Identify the blood parasite species.
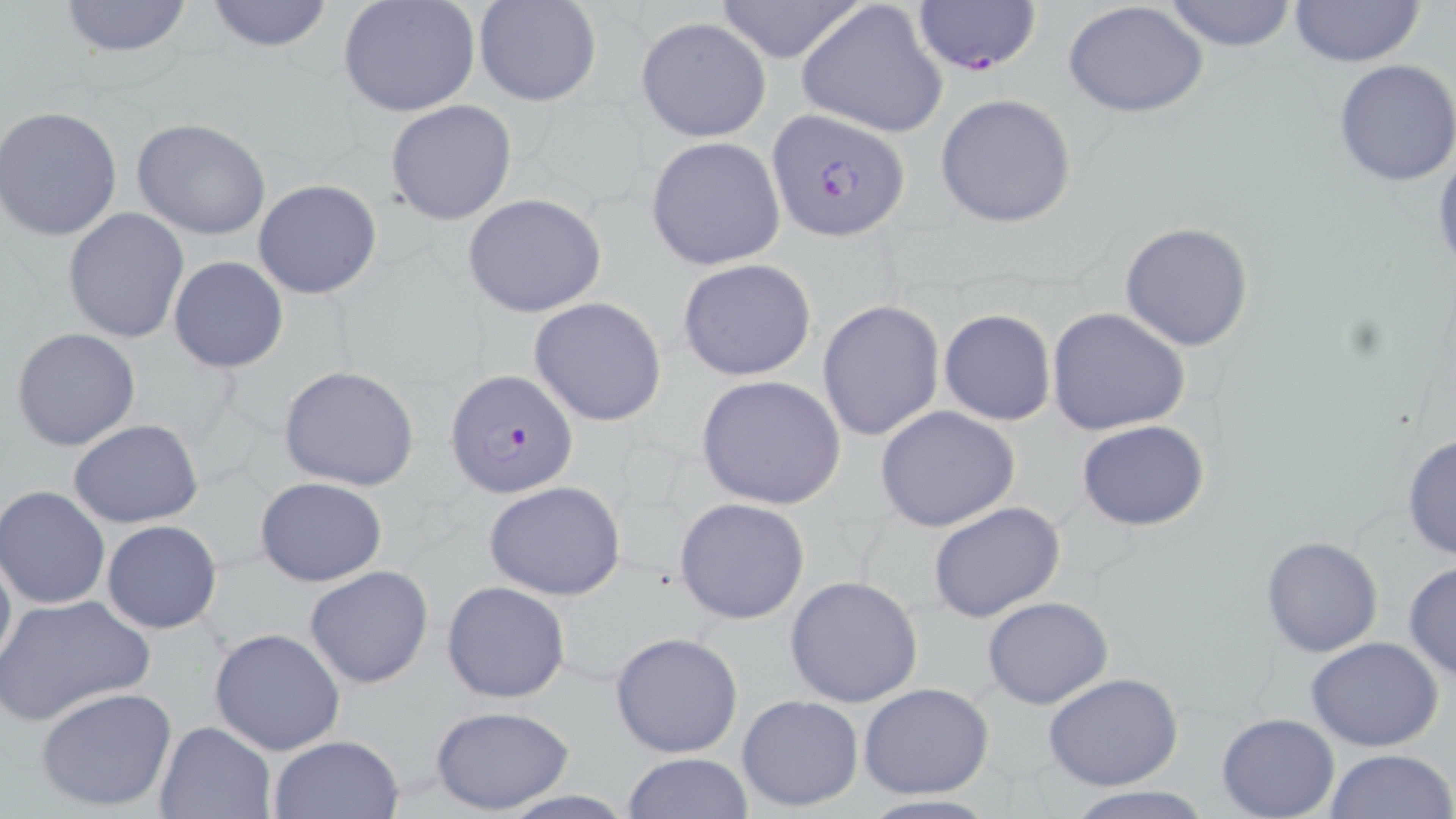
Plasmodium falciparum.

Approximate bounding boxes as (x1, y1, x2, y2) in pixels. Uninfected red blood cell locations: (56, 0, 196, 59), (204, 0, 334, 53), (338, 0, 480, 118), (474, 0, 602, 106), (708, 0, 869, 64), (796, 0, 950, 139), (1159, 0, 1300, 51), (1287, 0, 1426, 68), (1061, 1, 1212, 117), (636, 17, 770, 142), (1333, 59, 1456, 187), (935, 93, 1078, 228), (386, 99, 517, 226), (0, 105, 123, 243), (131, 119, 272, 241), (646, 137, 786, 271), (1431, 151, 1456, 280), (251, 179, 382, 300), (462, 193, 608, 318), (63, 207, 190, 343), (1119, 222, 1254, 351), (168, 257, 289, 372), (677, 258, 818, 382), (528, 297, 669, 427), (817, 298, 945, 440), (1046, 306, 1191, 436), (938, 309, 1055, 426), (10, 327, 142, 451), (278, 366, 419, 491), (695, 374, 847, 509), (875, 405, 1020, 532), (68, 419, 203, 528), (1076, 419, 1210, 531), (1403, 430, 1455, 563), (255, 477, 388, 587), (481, 480, 629, 602), (1, 485, 113, 611), (674, 497, 810, 624), (929, 502, 1066, 624), (101, 520, 223, 634), (1260, 535, 1384, 658), (0, 538, 15, 679), (1403, 560, 1456, 682), (303, 564, 434, 689), (784, 576, 924, 707), (441, 580, 571, 704), (0, 592, 155, 725), (981, 596, 1114, 708), (209, 627, 348, 755), (610, 632, 744, 758), (1305, 638, 1444, 752), (1044, 674, 1184, 791), (859, 682, 994, 800), (36, 687, 178, 813), (737, 693, 864, 813), (429, 705, 575, 814), (1216, 713, 1341, 819), (152, 720, 275, 819), (267, 734, 405, 818), (1322, 747, 1456, 819), (621, 752, 754, 818), (1065, 787, 1214, 818), (496, 789, 638, 818). Plasmodium falciparum-infected red blood cell locations: (913, 0, 1040, 74), (772, 108, 917, 239), (445, 368, 578, 500). May-Grünwald-Giemsa-stained preparation. Optical microscopy. 1000x magnification. Image is 1456×819 pixels. Thin blood film. Single field of view.